Name the cell type shown.
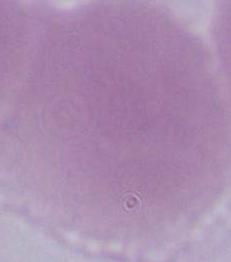
This is an erythrocyte.

Summary:
  - Magnification: 1000x
  - Modality: photomicrograph